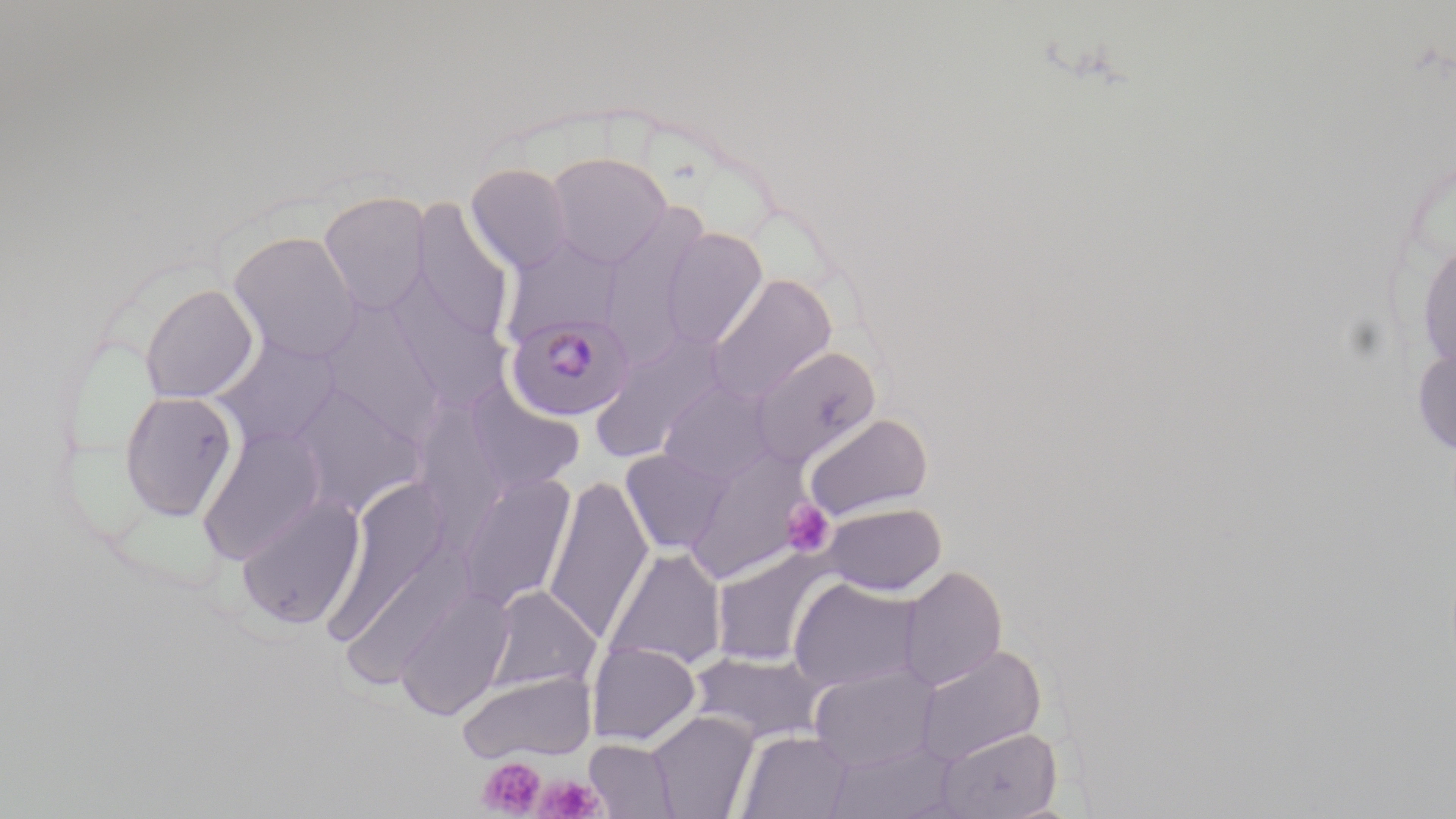

Approximate bounding boxes as named x1/y1/x2/y2 corners in pixels. Plasmodium malariae-infected red blood cell locations: (x1=505, y1=312, x2=635, y2=421). Platelet locations: (x1=781, y1=499, x2=836, y2=557), (x1=477, y1=756, x2=546, y2=817), (x1=536, y1=775, x2=603, y2=818). Uninfected red blood cell locations: (x1=545, y1=151, x2=672, y2=268), (x1=466, y1=163, x2=574, y2=274), (x1=318, y1=190, x2=432, y2=315), (x1=412, y1=202, x2=515, y2=342), (x1=600, y1=216, x2=705, y2=361), (x1=660, y1=227, x2=767, y2=350), (x1=228, y1=231, x2=361, y2=362), (x1=501, y1=235, x2=623, y2=344), (x1=1416, y1=235, x2=1455, y2=376), (x1=707, y1=273, x2=837, y2=404), (x1=390, y1=278, x2=513, y2=415), (x1=140, y1=283, x2=259, y2=404), (x1=317, y1=299, x2=446, y2=443), (x1=589, y1=334, x2=724, y2=462), (x1=214, y1=335, x2=342, y2=450), (x1=1412, y1=344, x2=1456, y2=455), (x1=751, y1=345, x2=881, y2=469), (x1=659, y1=380, x2=776, y2=485), (x1=290, y1=382, x2=428, y2=517), (x1=465, y1=383, x2=584, y2=496), (x1=118, y1=390, x2=238, y2=520), (x1=803, y1=413, x2=934, y2=521), (x1=197, y1=426, x2=327, y2=564), (x1=621, y1=448, x2=733, y2=556), (x1=683, y1=452, x2=815, y2=578), (x1=457, y1=473, x2=576, y2=612), (x1=542, y1=476, x2=654, y2=643), (x1=327, y1=481, x2=452, y2=647), (x1=236, y1=495, x2=366, y2=630), (x1=822, y1=502, x2=947, y2=595), (x1=605, y1=547, x2=727, y2=673), (x1=710, y1=547, x2=837, y2=667), (x1=898, y1=566, x2=1007, y2=692), (x1=788, y1=578, x2=923, y2=692), (x1=484, y1=585, x2=601, y2=696), (x1=396, y1=588, x2=514, y2=720), (x1=587, y1=642, x2=701, y2=746), (x1=913, y1=645, x2=1047, y2=766), (x1=688, y1=648, x2=827, y2=745), (x1=809, y1=665, x2=939, y2=771), (x1=456, y1=672, x2=596, y2=763), (x1=646, y1=711, x2=759, y2=819), (x1=936, y1=727, x2=1061, y2=819), (x1=736, y1=729, x2=853, y2=819), (x1=584, y1=738, x2=679, y2=818), (x1=823, y1=740, x2=959, y2=819). Slide-level diagnosis: Plasmodium malariae. Optical microscopy. May-Grünwald-Giemsa-stained preparation. One field of a larger specimen. Thin blood film. Captured at 1000x magnification. Image is 1456×819 pixels.